Name the parasite shown.
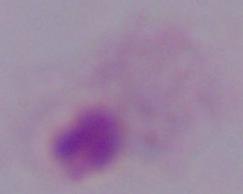
This is a trichomonad.

{
  "modality": "micrograph",
  "magnification": "1000x"
}